Assess this cell for malaria.
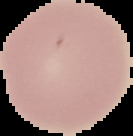

It is uninfected.

image size = 133×136 pixels
image type = segmented cell region on a black background
preparation = thin blood film